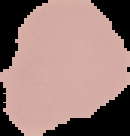

Image is 130×136 pixels. Segmented cell region on a black background. From a thin blood film. Result: negative for malaria parasites.